Assess this cell for malaria.
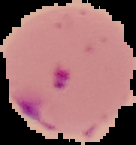

Parasitized.

Summary:
  - Image size: 136×145 pixels
  - Image type: cell region segmented out of the field of view; surrounding area masked to black
  - Preparation: thin blood film